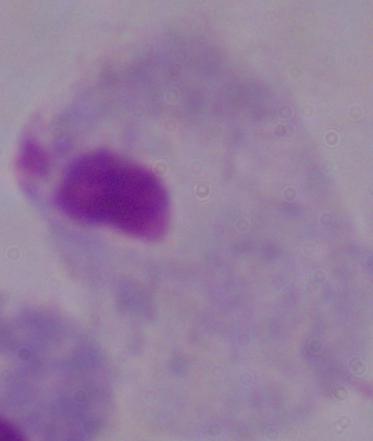
identification: trichomonad
modality: micrograph
magnification: 1000x